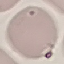

result: no malaria parasites seen
preparation: thin blood smear
image_type: automatically extracted cell patch, resized to 64 × 64 pixels
stain: Giemsa
capture: smartphone camera at the microscope eyepiece